State which parasite is depicted.
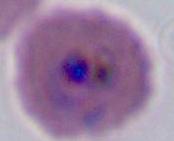
This is Plasmodium.

Summary:
  - Modality: micrograph
  - Magnification: 400x or 1000x